State which parasite is depicted.
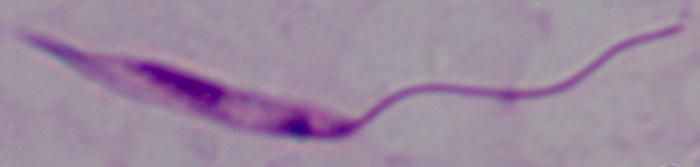

This is Leishmania.

Summary:
  - Magnification: 1000x
  - Modality: micrograph